Look for parasitized red blood cells.
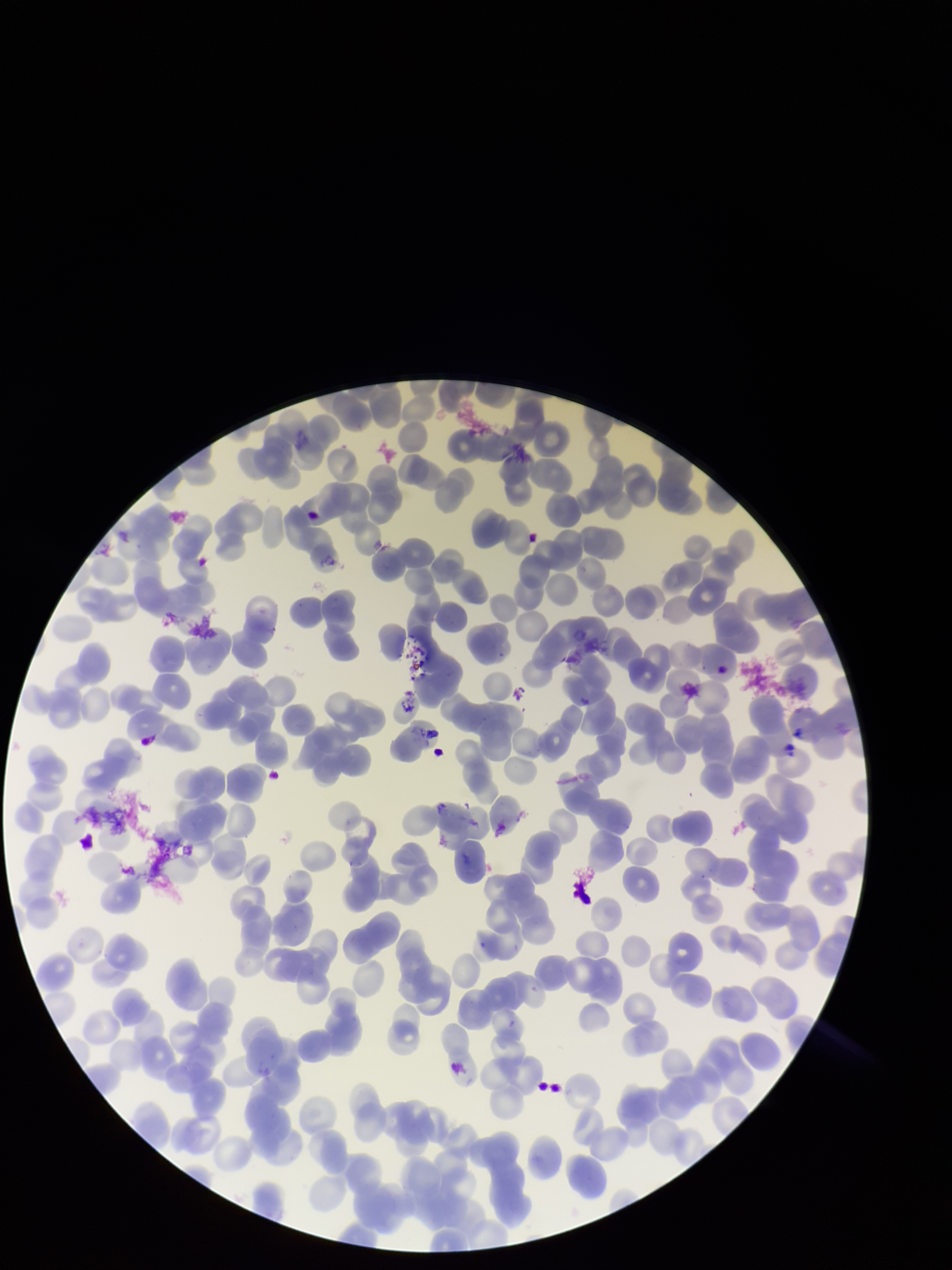
None seen.

Summary:
  - Stain: Giemsa
  - Red blood cell count: 211
  - Image size: 952×1270 pixels
  - Capture: smartphone photograph through the microscope eyepiece
  - Patient malaria status: infected
  - Species reported for this patient: Plasmodium falciparum
  - Field of view: single
  - Parasitized red blood cell count: 0
  - Preparation: thin